Identify the blood parasite species.
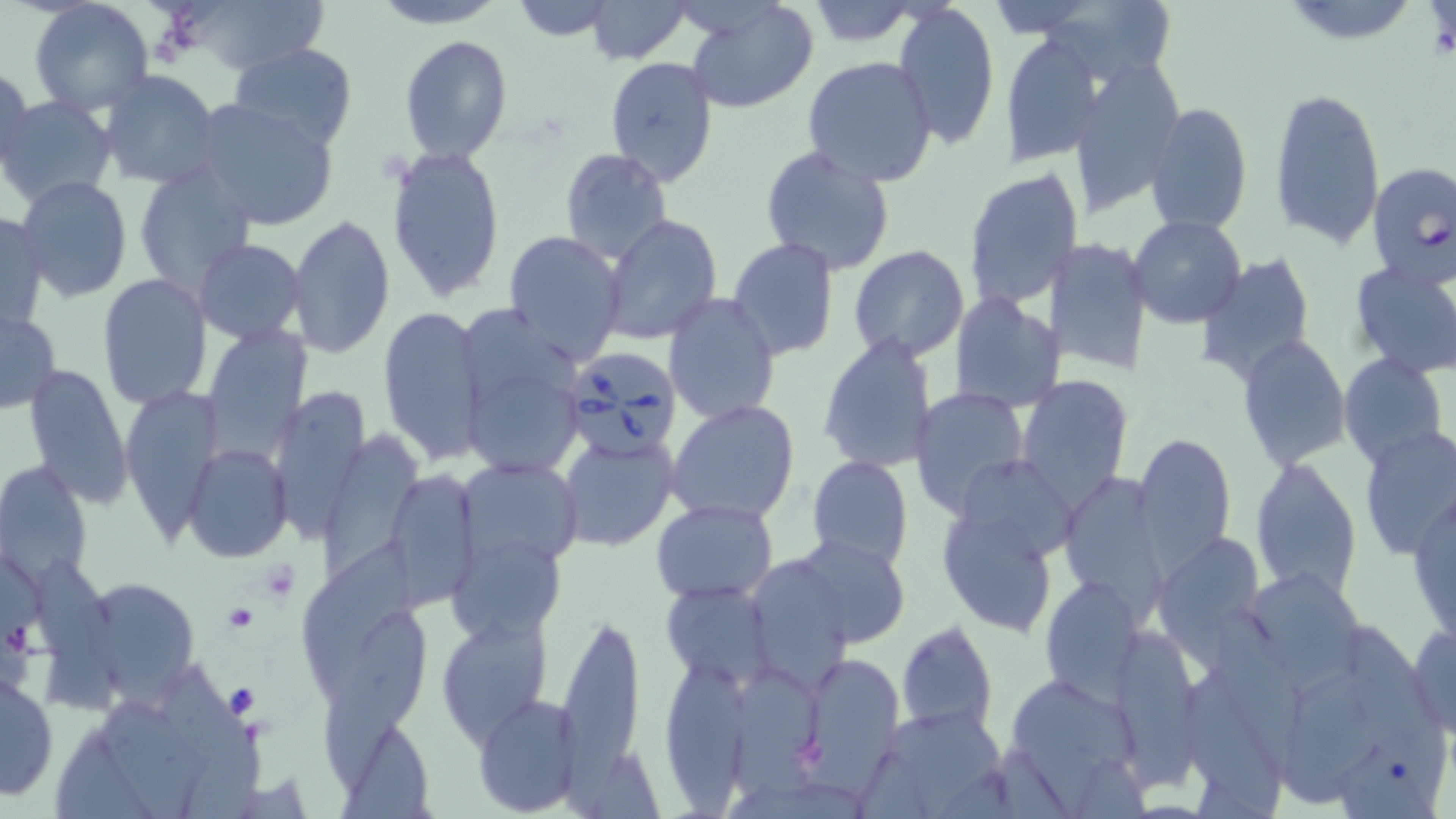
Babesia divergens.

Summary:
  - Coordinate format: approximate bounding boxes as (x1,y1)-(x2,y2) corner pairs in pixels
  - Babesia divergens-infected red blood cell locations: (1368,162)-(1456,289), (561,344)-(682,456)
  - Platelet locations: (257,558)-(300,599), (222,603)-(257,634)
  - Uninfected red blood cell locations: (183,0)-(335,74), (369,0)-(506,28), (507,0)-(620,42), (586,0)-(693,65), (1279,0)-(1424,49), (29,1)-(154,118), (686,1)-(818,115), (804,2)-(920,48), (894,2)-(1000,149), (1046,2)-(1177,82), (1000,30)-(1102,167), (399,35)-(514,165), (227,41)-(360,152), (801,56)-(938,187), (605,57)-(717,185), (1066,57)-(1186,212), (1,66)-(33,178), (97,70)-(221,190), (1269,85)-(1386,248), (2,95)-(116,209), (189,96)-(339,232), (1145,102)-(1253,234), (387,146)-(506,302), (759,146)-(896,277), (558,148)-(672,263), (132,163)-(256,294), (963,166)-(1083,310), (15,176)-(133,301), (0,211)-(48,331), (287,215)-(395,358), (601,215)-(722,344), (1129,216)-(1247,329), (503,231)-(626,366), (193,237)-(303,345), (727,237)-(839,360), (1044,237)-(1152,375), (848,247)-(970,363), (1196,252)-(1316,379), (1350,260)-(1456,380), (98,274)-(211,411), (663,293)-(780,425), (950,293)-(1068,412), (378,304)-(487,464), (458,304)-(584,403), (1,308)-(60,413), (206,321)-(312,463), (820,334)-(936,473), (1238,335)-(1352,470), (1338,352)-(1449,469), (459,360)-(590,485), (25,362)-(134,508), (1016,375)-(1134,510), (275,380)-(375,544), (120,385)-(224,550), (910,387)-(1031,517), (667,399)-(801,524), (1356,426)-(1456,563), (327,430)-(428,585), (557,432)-(678,553), (1134,432)-(1236,568), (187,443)-(292,562), (807,456)-(913,568), (456,458)-(583,569), (1250,458)-(1361,598), (0,461)-(94,583), (953,461)-(1075,565), (382,467)-(479,609), (1061,471)-(1166,618), (1411,482)-(1455,651), (651,497)-(778,601), (937,503)-(1063,639), (447,529)-(565,644), (791,535)-(909,646), (1152,537)-(1270,675), (305,543)-(420,683), (749,557)-(858,694), (33,560)-(125,714), (1248,568)-(1360,679), (72,571)-(203,702), (1040,576)-(1144,703), (660,579)-(775,690), (1212,607)-(1312,778), (553,610)-(646,782), (318,611)-(435,794), (436,612)-(553,745), (1344,617)-(1449,814), (1109,619)-(1205,791), (897,621)-(999,735), (1408,621)-(1455,735), (796,649)-(908,788), (657,653)-(759,809), (727,659)-(831,805), (160,669)-(256,762), (1182,669)-(1283,819), (0,671)-(57,801), (1286,671)-(1382,807), (1002,675)-(1139,793), (473,693)-(585,817), (105,700)-(213,819), (873,705)-(1008,813), (53,723)-(157,819), (346,727)-(436,819)
  - Magnification: 1000x
  - Modality: light microscopy
  - Field of view: one of a larger specimen
  - Preparation: thin blood smear
  - Stain: May-Grünwald-Giemsa
  - Image size: 1456×819 pixels